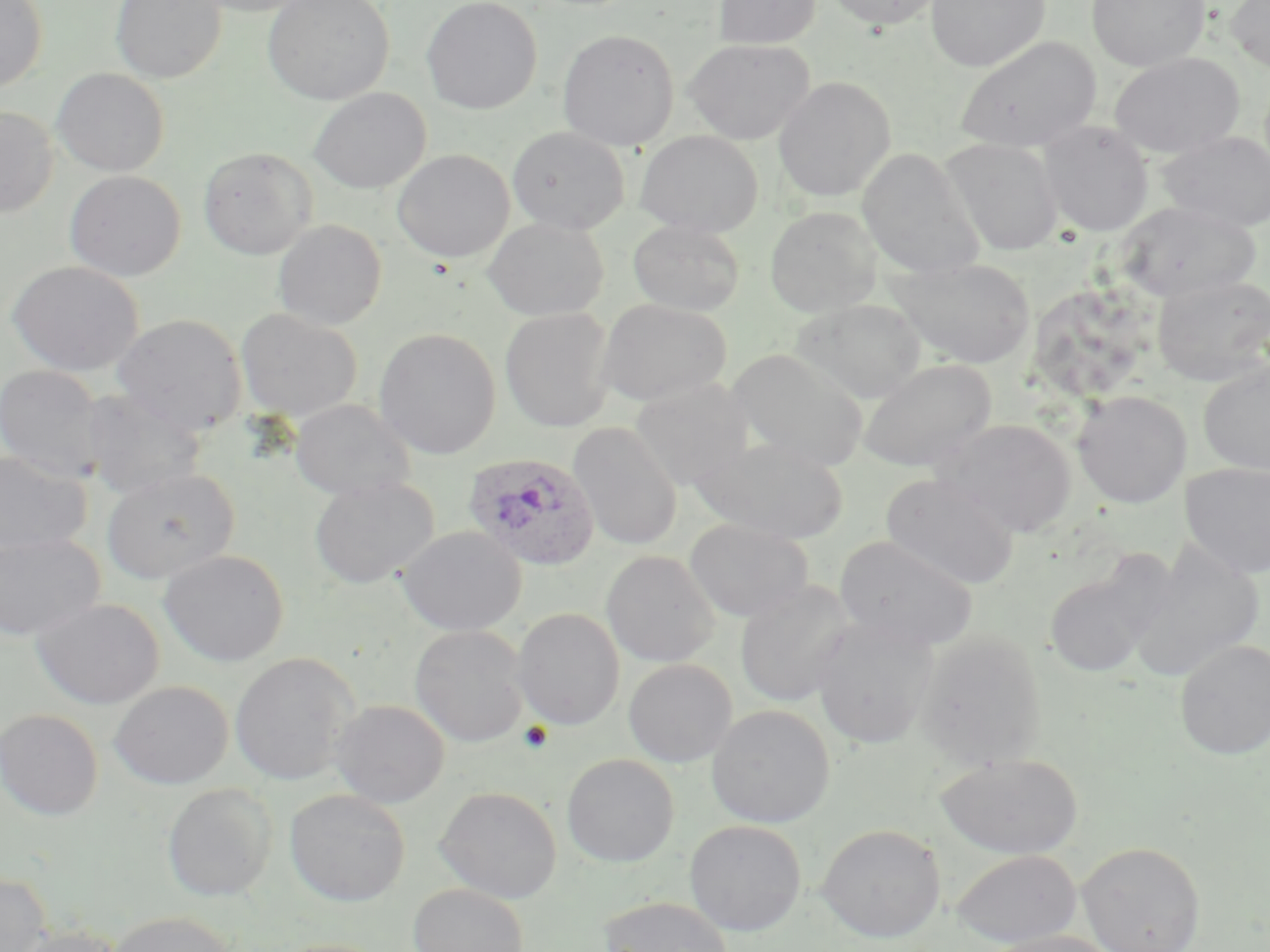

Approximate bounding boxes as (x1, y1, x2, y2) in pixels. Plasmodium ovale-infected red blood cell locations: (463, 451, 602, 571). Platelet locations: (518, 721, 554, 754). Uninfected red blood cell locations: (0, 0, 47, 92), (110, 0, 227, 84), (186, 0, 318, 16), (263, 0, 394, 104), (421, 0, 542, 114), (713, 0, 821, 49), (823, 0, 943, 29), (925, 0, 1050, 71), (1087, 0, 1210, 71), (1226, 0, 1270, 71), (557, 29, 680, 151), (955, 35, 1101, 153), (683, 38, 814, 145), (1109, 52, 1245, 158), (51, 68, 169, 176), (773, 76, 895, 202), (308, 87, 430, 194), (0, 105, 58, 218), (1038, 120, 1154, 236), (507, 126, 630, 234), (635, 130, 764, 237), (1157, 131, 1270, 231), (940, 137, 1064, 256), (198, 147, 317, 259), (857, 147, 984, 279), (392, 149, 514, 262), (64, 170, 186, 281), (1115, 201, 1261, 304), (764, 206, 881, 317), (483, 216, 609, 320), (273, 219, 387, 330), (627, 219, 744, 316), (884, 257, 1037, 369), (7, 261, 144, 377), (1151, 274, 1270, 387), (1037, 281, 1150, 402), (595, 298, 732, 406), (794, 298, 926, 403), (500, 307, 617, 432), (236, 308, 363, 421), (742, 308, 911, 443), (112, 313, 248, 437), (374, 328, 501, 459), (727, 348, 869, 472), (858, 359, 997, 472), (874, 359, 1004, 588), (1198, 360, 1270, 475), (0, 363, 106, 482), (630, 378, 753, 491), (79, 388, 206, 500), (1073, 390, 1191, 508), (290, 398, 416, 501), (934, 418, 1077, 537), (567, 421, 683, 551), (692, 437, 850, 543), (0, 449, 91, 557), (1180, 461, 1270, 578), (101, 467, 239, 585), (880, 473, 1020, 590), (309, 476, 439, 589), (685, 517, 813, 622), (398, 526, 526, 635), (0, 532, 105, 642), (834, 535, 978, 651), (1125, 540, 1266, 681), (159, 549, 290, 667), (601, 550, 720, 667), (1044, 568, 1158, 678), (734, 579, 858, 708), (31, 597, 164, 709), (512, 608, 625, 731), (811, 618, 938, 748), (409, 625, 530, 747), (916, 630, 1047, 768), (1174, 638, 1270, 760), (230, 652, 359, 786), (623, 658, 737, 767), (110, 680, 233, 789), (330, 699, 450, 808), (706, 704, 835, 827), (0, 708, 103, 820), (935, 753, 1083, 859), (561, 754, 679, 867), (162, 783, 277, 901), (435, 786, 562, 904), (285, 788, 410, 906), (684, 820, 806, 936), (817, 823, 945, 942), (1076, 841, 1206, 952), (951, 848, 1081, 947), (0, 873, 51, 952), (408, 883, 529, 952), (599, 896, 735, 952), (106, 910, 237, 952), (8, 926, 125, 952), (981, 929, 1121, 952), (267, 938, 390, 952). Slide-level diagnosis: Plasmodium ovale. One field of a larger specimen. May-Grünwald-Giemsa stain. Thin blood film. Captured at 1000x magnification. Image is 1270×952 pixels. Light microscopy.